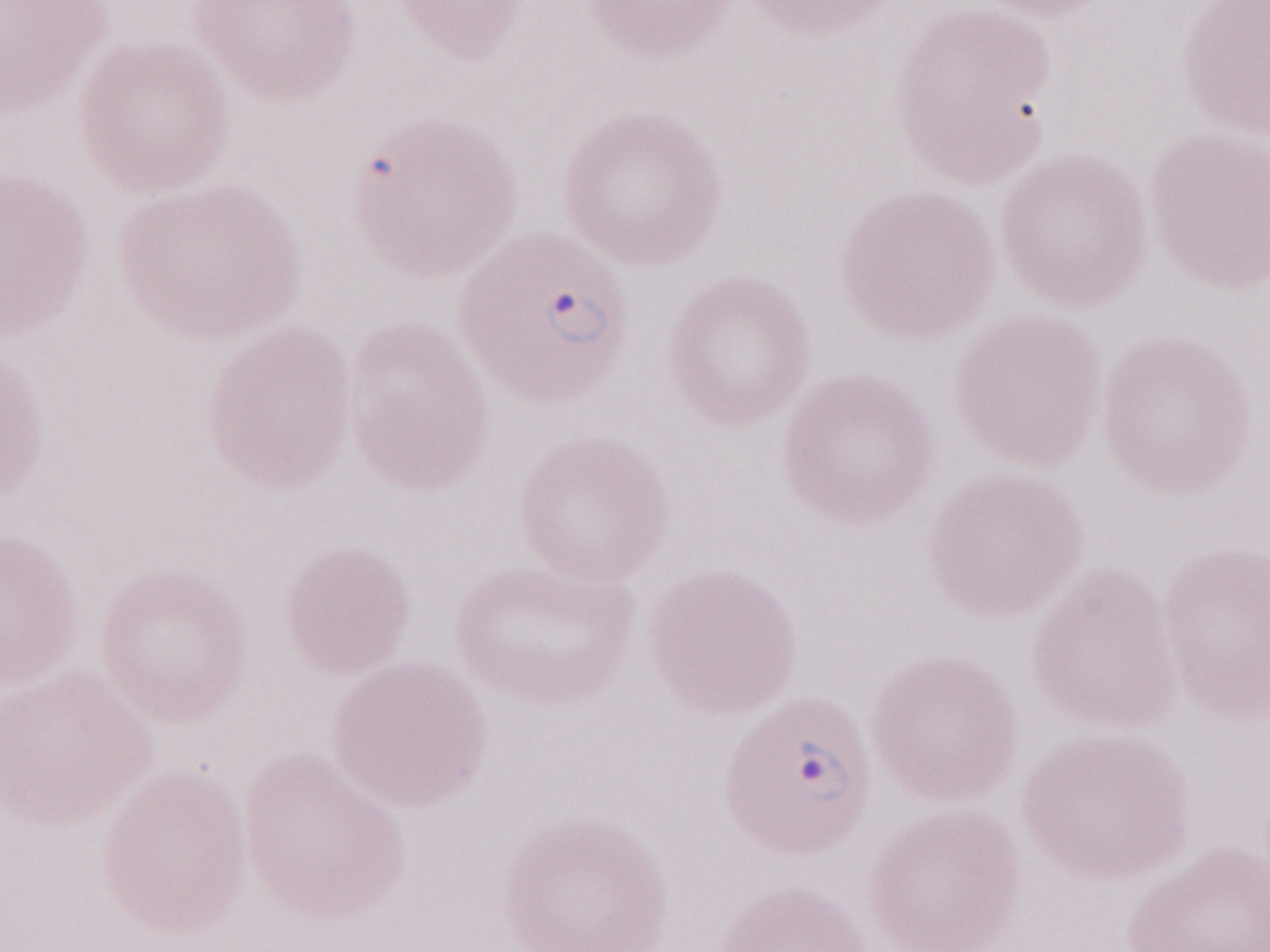

Thin blood film. One field of this slide. Image is 1270×952 pixels. May-Grünwald-Giemsa stain. Olympus BX43 microscope and DP73 digital camera. Magnification: 1,000x. Patient diagnosis: malaria infection.